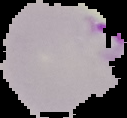

Result: malaria parasites detected. The area outside the segmented cell region is set to black. Image is 127×118 pixels. From a thin blood film.